State which cell type is depicted.
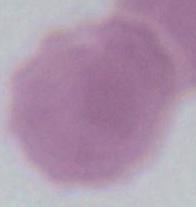

An erythrocyte.

magnification = 1000x
modality = micrograph